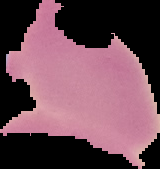

Summary:
  - Malaria status: uninfected
  - Image size: 160×169 pixels
  - Preparation: thin blood film
  - Image type: segmented cell region on a black background